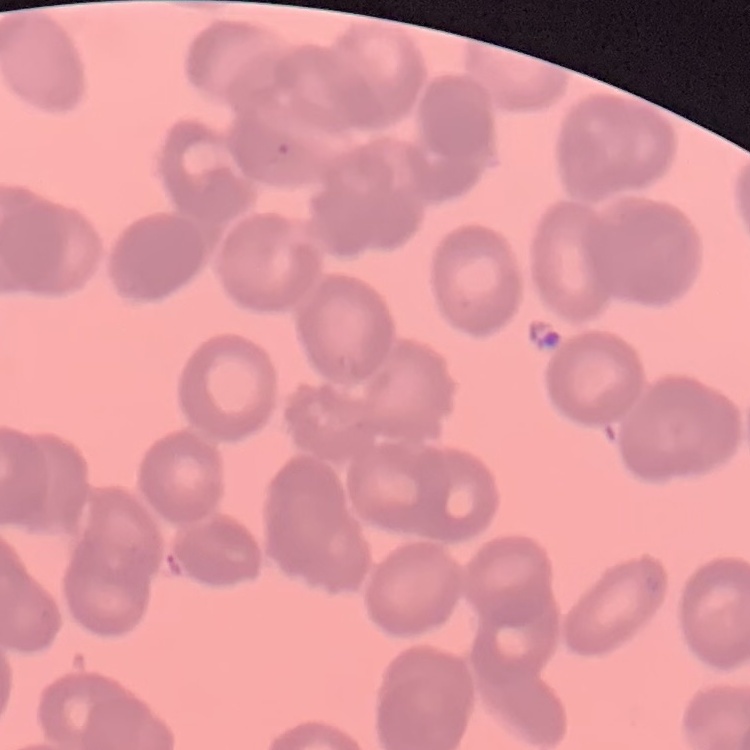
red blood cell morphology = rouleaux formation
image type = one tile cut from a larger photomicrograph
preparation = thin peripheral smear
stain = Field's or Giemsa